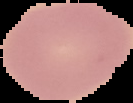

Cell region segmented out of the field of view; the surrounding area is masked to black. From a thin blood film. Malaria status: uninfected. Image is 133×103 pixels.